Report the malaria status of this cell.
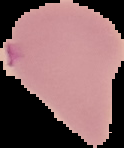

Parasitized.

image size = 124×148 pixels
image type = cell region segmented out of the field of view; surrounding area masked to black
preparation = thin blood smear